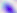

Toxoplasma gondii is shown. Captured at 400x magnification. Micrograph.